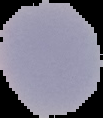
The area outside the segmented cell region is set to black. From a thin blood smear. Image is 103×118 pixels. Result: no Plasmodium parasites detected.